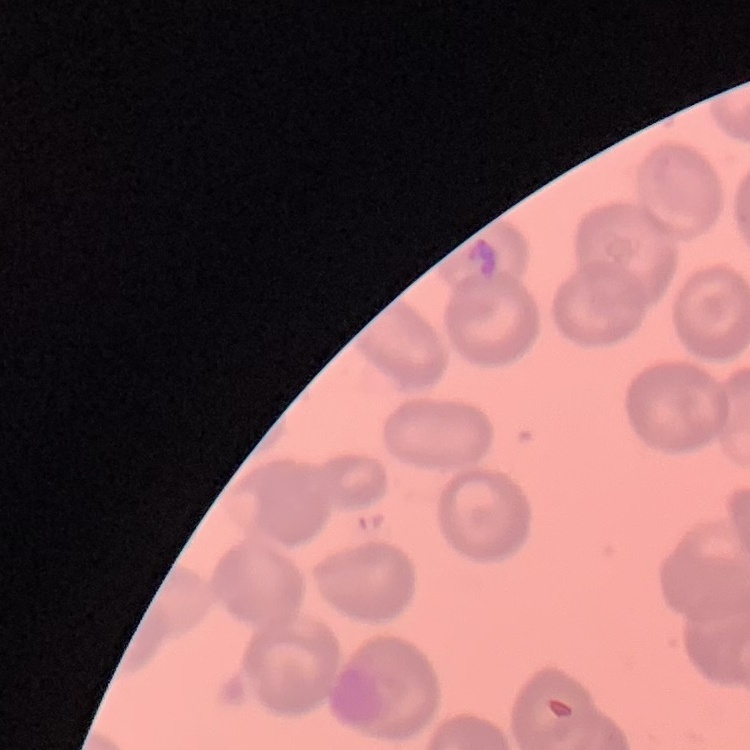
Summary:
  - Red blood cell morphology: no rouleaux formation
  - Image type: square crop of a larger photomicrograph
  - Preparation: thin blood smear
  - Stain: Field's or Giemsa